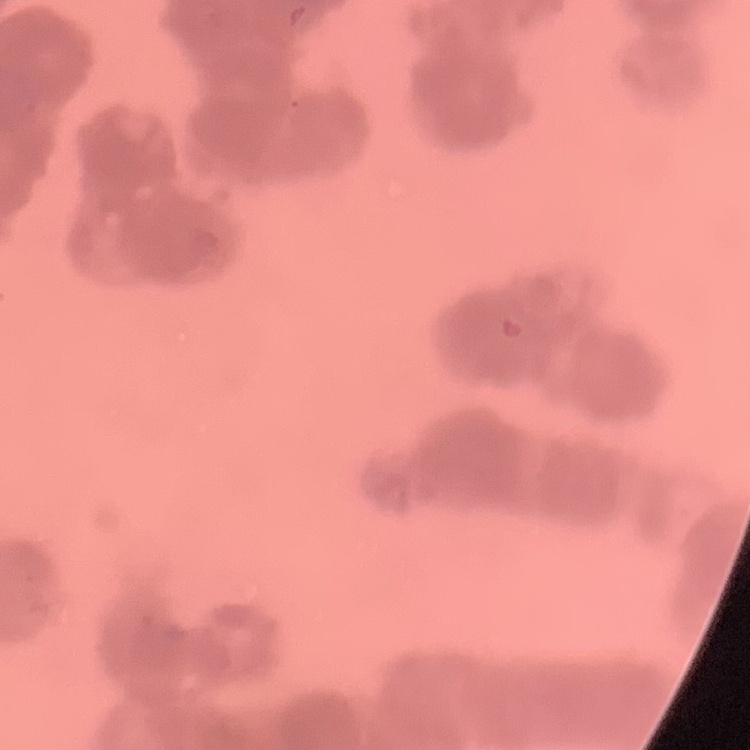
red blood cell morphology = rouleaux formation
preparation = thin blood film
image type = square crop of a larger photomicrograph
stain = Field's or Giemsa